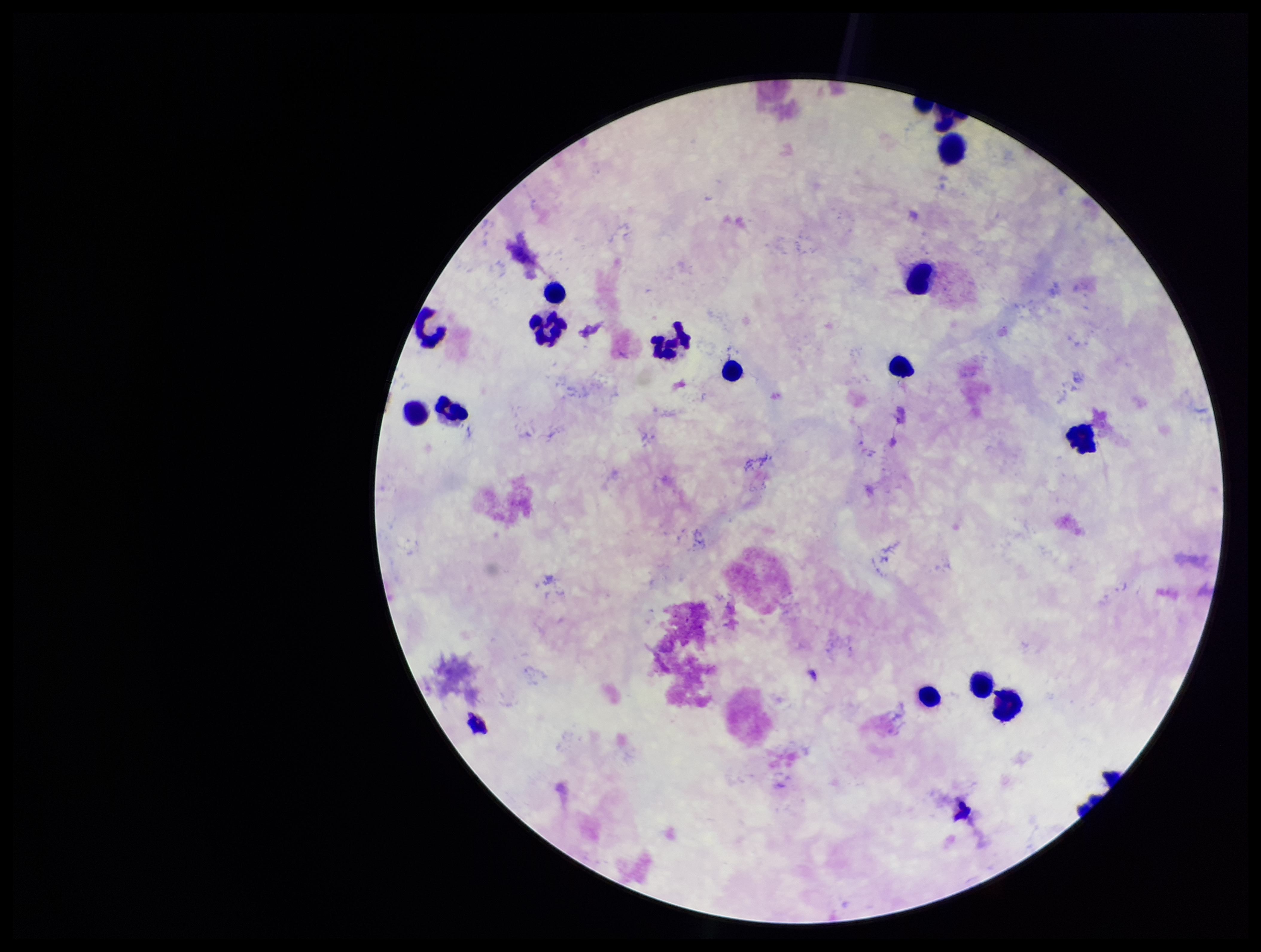

Summary:
  - Parasite count: 0
  - Capture: smartphone photograph through the microscope eyepiece
  - Field of view: single
  - Leukocyte count: 14
  - Patient malaria status: negative
  - Plasmodium parasites: none identified
  - Stain: Giemsa
  - Image size: 1261×952 pixels
  - Preparation: thick smear